Report the malaria status of this cell.
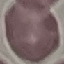

It is uninfected.

Summary:
  - Image type: automatically extracted cell patch, resized to 64 × 64 pixels
  - Capture: smartphone through the microscope eyepiece
  - Stain: Giemsa
  - Preparation: thin blood smear